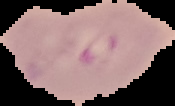
Summary:
  - Image type: cell region segmented out of the field of view; surrounding area masked to black
  - Malaria status: parasitized
  - Preparation: thin blood smear
  - Image size: 175×106 pixels